Classify this cell by malaria status.
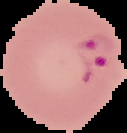
Parasitized.

Segmented cell region on a black background. Image is 127×133 pixels. From a thin blood smear.